Assess this cell for malaria.
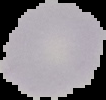
Uninfected.

preparation = thin blood film
image type = segmented cell region with the area outside set to black
image size = 106×100 pixels